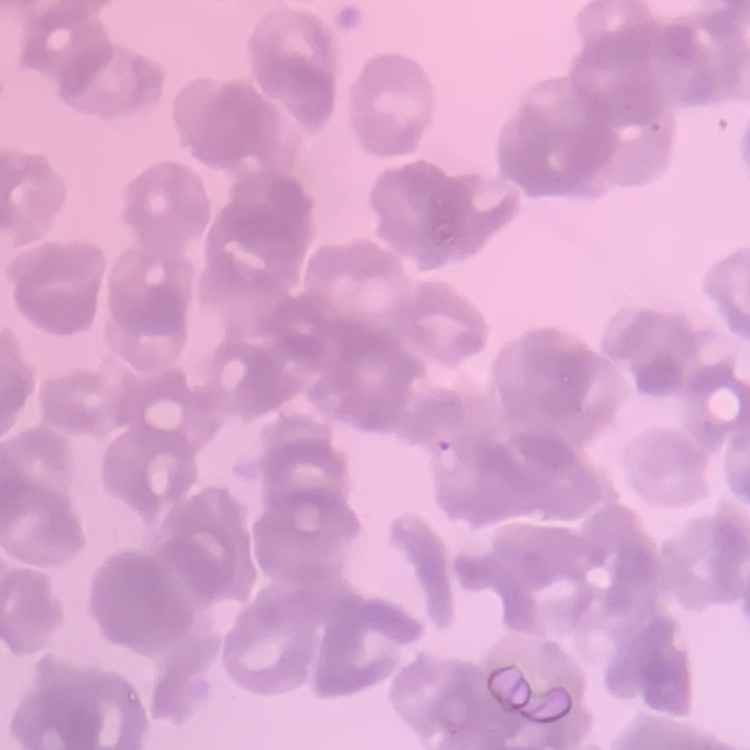
{
  "erythrocyte_morphology": "rouleaux formation",
  "preparation": "thin blood smear",
  "stain": "Field's or Giemsa",
  "image_type": "one tile cut from a larger photomicrograph"
}